Assess this cell for malaria.
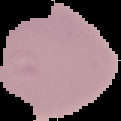
Uninfected.

Summary:
  - Image type: segmented cell region with the area outside set to black
  - Image size: 121×121 pixels
  - Preparation: thin blood film